Assess the morphology of the erythrocytes.
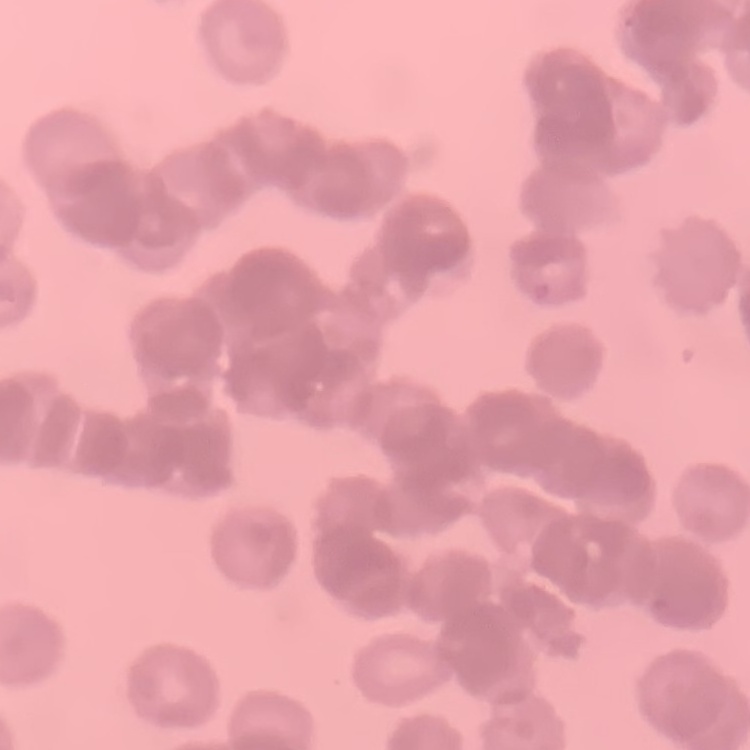

They show rouleaux formation.

Thin blood smear. Field's or Giemsa stain. Square crop of a larger photomicrograph.